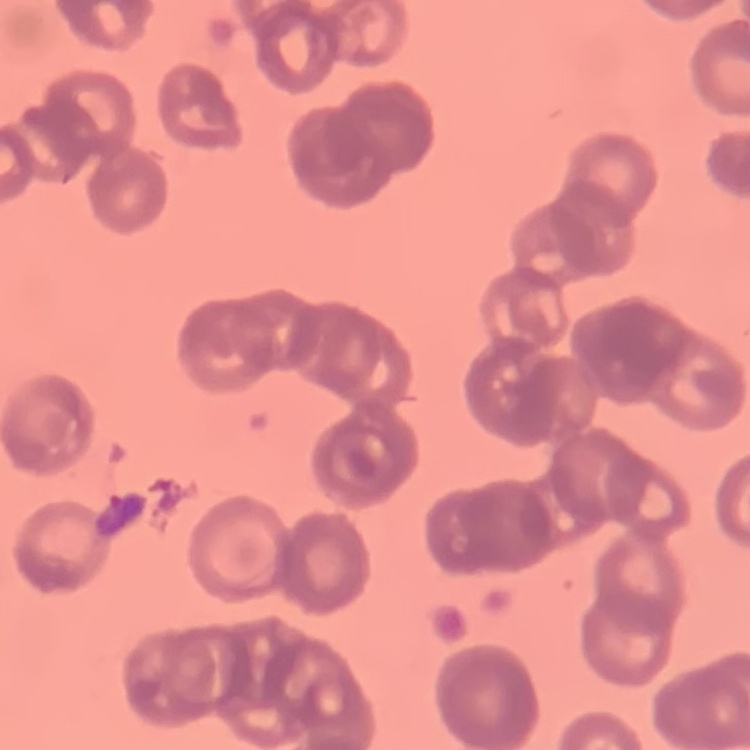
Summary:
  - Erythrocyte morphology: rouleaux formation
  - Preparation: thin blood smear
  - Image type: one tile cut from a larger photomicrograph
  - Stain: Field's or Giemsa